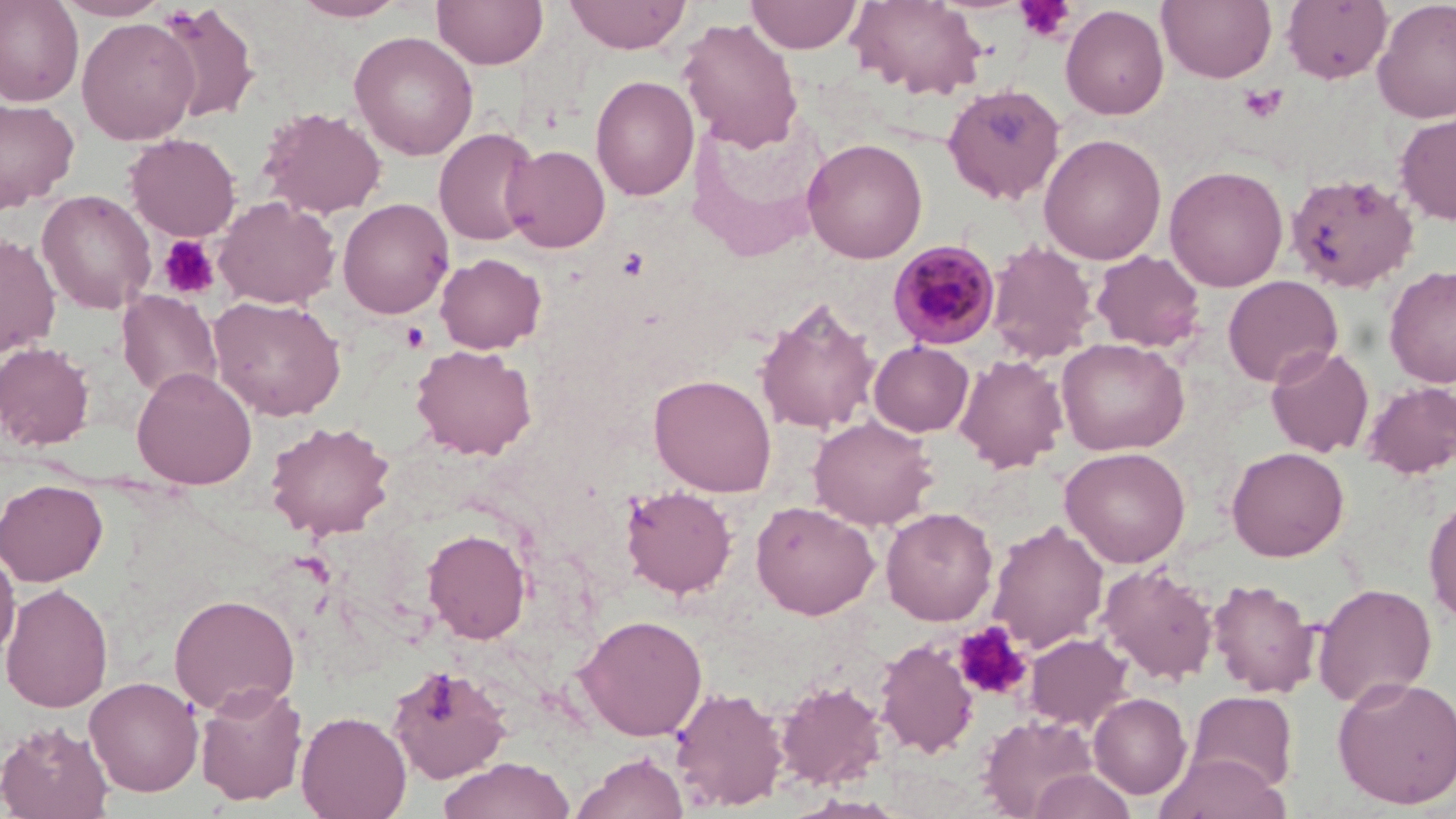
Approximate bounding boxes as named x1/y1/x2/y2 corners in pixels. Plasmodium malariae-infected red blood cell locations: (x1=887, y1=239, x2=1001, y2=349). Uninfected red blood cell locations: (x1=0, y1=0, x2=84, y2=108), (x1=54, y1=0, x2=171, y2=21), (x1=292, y1=0, x2=408, y2=22), (x1=432, y1=0, x2=548, y2=69), (x1=564, y1=0, x2=690, y2=54), (x1=746, y1=0, x2=862, y2=53), (x1=846, y1=0, x2=988, y2=100), (x1=1157, y1=0, x2=1276, y2=83), (x1=1282, y1=0, x2=1392, y2=84), (x1=1372, y1=0, x2=1456, y2=123), (x1=155, y1=4, x2=261, y2=124), (x1=1060, y1=4, x2=1169, y2=120), (x1=77, y1=17, x2=199, y2=144), (x1=677, y1=18, x2=804, y2=151), (x1=349, y1=31, x2=478, y2=161), (x1=590, y1=75, x2=699, y2=201), (x1=942, y1=82, x2=1066, y2=204), (x1=0, y1=97, x2=79, y2=212), (x1=259, y1=107, x2=387, y2=219), (x1=1395, y1=112, x2=1456, y2=226), (x1=434, y1=127, x2=540, y2=246), (x1=125, y1=132, x2=242, y2=241), (x1=1038, y1=133, x2=1167, y2=264), (x1=802, y1=138, x2=927, y2=263), (x1=503, y1=145, x2=611, y2=253), (x1=1164, y1=165, x2=1289, y2=291), (x1=1286, y1=172, x2=1420, y2=292), (x1=37, y1=190, x2=156, y2=315), (x1=213, y1=197, x2=341, y2=309), (x1=337, y1=198, x2=454, y2=319), (x1=0, y1=233, x2=61, y2=358), (x1=985, y1=240, x2=1098, y2=363), (x1=1091, y1=250, x2=1207, y2=352), (x1=434, y1=253, x2=547, y2=354), (x1=1385, y1=265, x2=1456, y2=388), (x1=1223, y1=275, x2=1343, y2=387), (x1=117, y1=290, x2=222, y2=399), (x1=208, y1=295, x2=347, y2=421), (x1=755, y1=297, x2=880, y2=436), (x1=1057, y1=338, x2=1190, y2=456), (x1=869, y1=341, x2=974, y2=437), (x1=0, y1=342, x2=95, y2=450), (x1=411, y1=344, x2=537, y2=460), (x1=1265, y1=345, x2=1374, y2=458), (x1=954, y1=354, x2=1069, y2=473), (x1=131, y1=367, x2=257, y2=490), (x1=648, y1=373, x2=777, y2=497), (x1=1361, y1=381, x2=1456, y2=479), (x1=808, y1=416, x2=938, y2=530), (x1=265, y1=420, x2=395, y2=541), (x1=1060, y1=445, x2=1191, y2=567), (x1=1226, y1=447, x2=1349, y2=561), (x1=0, y1=478, x2=108, y2=586), (x1=621, y1=486, x2=737, y2=599), (x1=1423, y1=491, x2=1456, y2=626), (x1=751, y1=500, x2=879, y2=619), (x1=881, y1=507, x2=998, y2=625), (x1=987, y1=520, x2=1109, y2=653), (x1=422, y1=527, x2=532, y2=644), (x1=0, y1=545, x2=20, y2=663), (x1=1097, y1=562, x2=1219, y2=685), (x1=1208, y1=578, x2=1321, y2=698), (x1=1, y1=582, x2=113, y2=713), (x1=1313, y1=582, x2=1437, y2=708), (x1=169, y1=593, x2=300, y2=716), (x1=574, y1=614, x2=707, y2=741), (x1=1024, y1=633, x2=1133, y2=731), (x1=874, y1=639, x2=979, y2=758), (x1=386, y1=663, x2=513, y2=784), (x1=1332, y1=675, x2=1456, y2=809), (x1=84, y1=676, x2=203, y2=797), (x1=196, y1=680, x2=309, y2=806), (x1=775, y1=681, x2=887, y2=789), (x1=669, y1=684, x2=789, y2=811), (x1=1187, y1=691, x2=1298, y2=793), (x1=1088, y1=693, x2=1191, y2=799), (x1=295, y1=710, x2=411, y2=819), (x1=979, y1=714, x2=1099, y2=817), (x1=0, y1=720, x2=114, y2=819), (x1=1153, y1=751, x2=1289, y2=819), (x1=571, y1=752, x2=690, y2=819), (x1=438, y1=756, x2=575, y2=819), (x1=1027, y1=768, x2=1136, y2=818). Platelet locations: (x1=1016, y1=0, x2=1074, y2=42), (x1=1238, y1=83, x2=1288, y2=124), (x1=157, y1=235, x2=220, y2=301), (x1=400, y1=322, x2=429, y2=352), (x1=954, y1=621, x2=1032, y2=700). Slide-level diagnosis: Plasmodium malariae. May-Grünwald-Giemsa stain. Single field of view. Thin blood smear. 1000x magnification. Optical microscopy. Image is 1456×819 pixels.